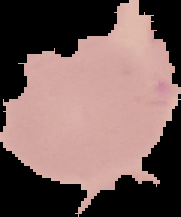
{
  "malaria_status": "uninfected",
  "preparation": "thin blood smear",
  "image_type": "cell region segmented out of the field of view; surrounding area masked to black",
  "image_size": "181×217 pixels"
}